Report the malaria status of this cell.
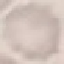

It is uninfected.

preparation = thin smear
image type = automatically extracted cell patch, resized to 64 × 64 pixels
capture = smartphone through the microscope eyepiece
stain = Giemsa